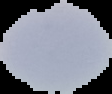

Summary:
  - Image size: 112×94 pixels
  - Result: no Plasmodium parasites seen
  - Preparation: thin blood film
  - Image type: segmented cell region with the area outside set to black